Describe the morphology of the erythrocytes.
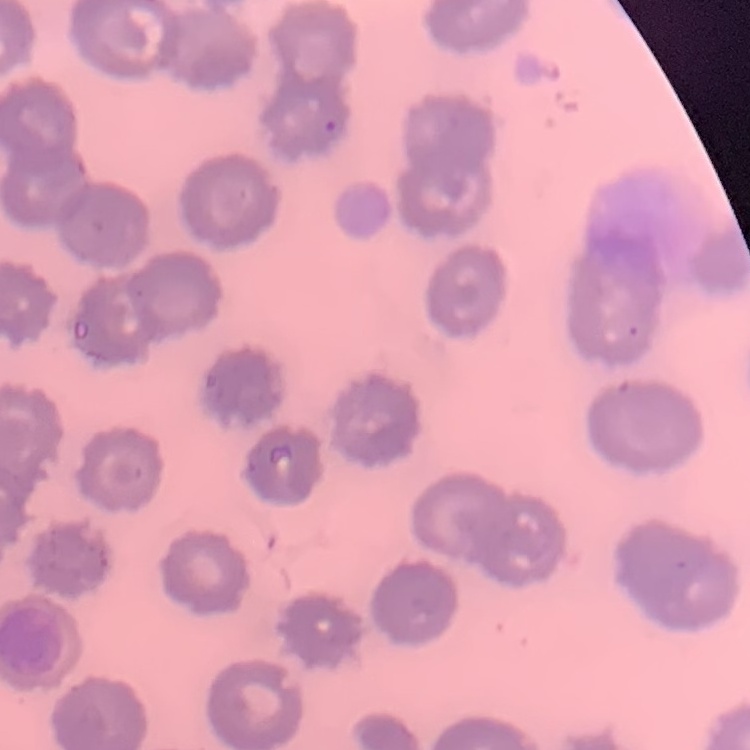

No rouleaux formation.

Summary:
  - Preparation: thin peripheral smear
  - Stain: Field's or Giemsa
  - Image type: square crop of a larger photomicrograph